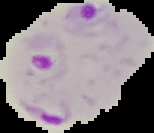 Cell region segmented out of the field of view; the surrounding area is masked to black. From a thin blood smear. Image is 154×133 pixels. Result: malaria parasites identified.